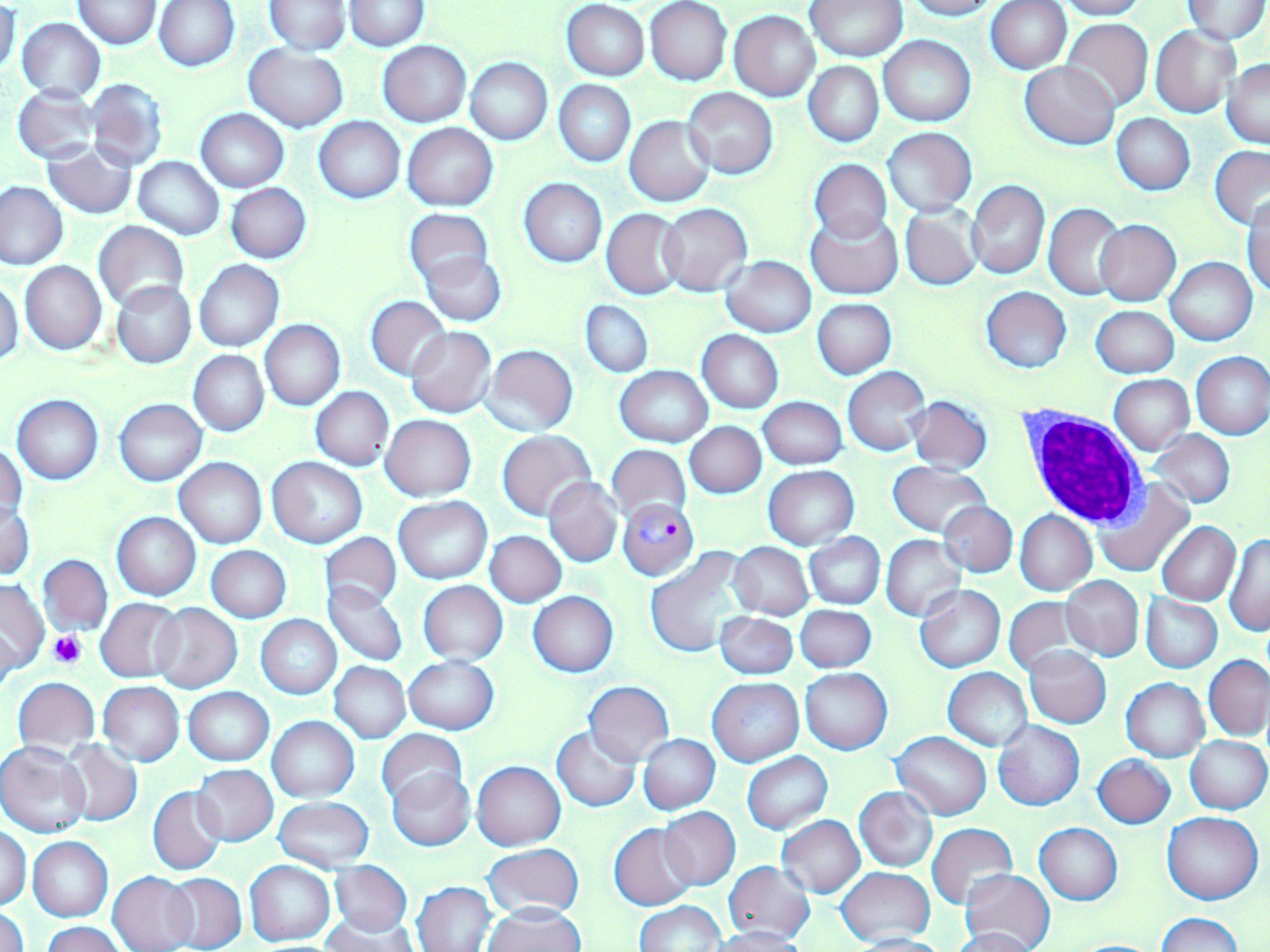
Summary:
  - Coordinate format: approximate bounding boxes as (x1,y1)-(x2,y2) corner pairs in pixels
  - Uninfected red blood cell locations: (73,0)-(162,49), (263,0)-(352,54), (806,0)-(908,63), (901,0)-(1000,20), (1054,0)-(1149,19), (154,1)-(240,72), (344,1)-(429,50), (986,1)-(1070,73), (1181,1)-(1270,43), (563,2)-(649,80), (645,2)-(732,85), (0,4)-(21,81), (729,11)-(820,101), (17,17)-(105,103), (1061,19)-(1154,111), (1151,26)-(1239,118), (878,36)-(975,127), (378,41)-(471,127), (244,45)-(348,131), (466,58)-(552,144), (1224,59)-(1269,147), (805,61)-(883,146), (1021,61)-(1119,150), (85,78)-(169,172), (554,81)-(635,166), (12,86)-(100,163), (681,87)-(778,179), (197,108)-(288,192), (1112,114)-(1194,195), (625,116)-(715,206), (315,117)-(404,203), (403,123)-(497,211), (881,127)-(977,216), (41,141)-(138,218), (1209,147)-(1270,228), (133,156)-(224,239), (809,159)-(893,243), (518,179)-(607,268), (965,179)-(1051,280), (0,181)-(68,270), (226,183)-(312,262), (1245,199)-(1270,299), (659,203)-(752,294), (1044,203)-(1127,299), (901,204)-(982,290), (601,208)-(685,298), (404,209)-(493,292), (806,211)-(901,299), (1095,219)-(1181,306), (93,221)-(189,311), (420,249)-(505,325), (1165,257)-(1257,345), (721,258)-(816,338), (193,259)-(285,352), (20,261)-(107,354), (0,278)-(23,368), (112,281)-(196,369), (981,288)-(1073,372), (366,296)-(450,380), (812,299)-(896,378), (581,301)-(653,377), (1091,305)-(1179,378), (259,319)-(346,410), (404,326)-(496,418), (698,331)-(783,413), (482,345)-(578,437), (188,350)-(269,436), (1192,351)-(1270,440), (615,366)-(712,447), (843,367)-(930,455), (1110,374)-(1194,455), (299,386)-(384,543), (311,387)-(394,471), (12,395)-(104,484), (909,395)-(994,476), (759,397)-(846,469), (115,398)-(207,485), (381,414)-(476,501), (685,421)-(766,498), (1148,429)-(1235,509), (497,431)-(595,520), (1,443)-(26,525), (607,445)-(691,523), (267,457)-(367,548), (174,458)-(266,548), (888,462)-(992,537), (763,466)-(859,548), (544,477)-(622,568), (1092,477)-(1195,578), (395,498)-(492,583), (938,502)-(1016,577), (1,503)-(34,580), (1015,510)-(1096,595), (112,512)-(200,600), (1157,521)-(1240,605), (486,531)-(566,606), (1223,531)-(1270,636), (321,532)-(402,613), (805,533)-(885,608), (881,533)-(966,621), (730,542)-(813,620), (207,546)-(291,622), (646,548)-(755,658), (38,554)-(113,637), (1060,576)-(1145,662), (1,579)-(49,673), (324,581)-(409,667), (418,581)-(507,665), (915,586)-(1005,672), (529,591)-(618,676), (1141,596)-(1222,672), (1003,597)-(1085,676), (96,598)-(185,682), (152,604)-(242,693), (795,606)-(876,672), (715,612)-(798,679), (255,615)-(341,699), (1,624)-(19,702), (1025,646)-(1111,727), (1205,655)-(1270,739), (403,656)-(498,733), (329,662)-(410,743), (800,667)-(892,754), (944,667)-(1032,751), (12,676)-(99,756), (707,677)-(804,766), (1120,678)-(1209,762), (583,681)-(675,766), (97,682)-(184,767), (183,687)-(273,765), (267,716)-(360,801), (993,720)-(1085,812), (552,726)-(641,811), (377,729)-(468,809), (892,732)-(991,819), (638,734)-(720,814), (1185,735)-(1268,814), (62,740)-(142,826), (1,743)-(90,838), (742,752)-(833,833), (1093,754)-(1176,828), (472,761)-(566,850), (191,765)-(277,846), (386,769)-(475,851), (149,786)-(226,876), (854,786)-(938,872), (274,797)-(373,872), (260,800)-(364,930), (660,808)-(741,889), (1163,812)-(1262,905), (777,815)-(865,898), (926,822)-(1018,909), (609,823)-(698,910), (1035,823)-(1122,905), (1,825)-(32,909), (27,837)-(113,921), (483,843)-(585,919), (245,859)-(336,945), (328,861)-(413,936), (722,861)-(815,943), (415,863)-(579,942), (837,867)-(934,944), (961,868)-(1056,952), (108,871)-(198,952), (164,872)-(246,952), (413,881)-(496,951), (634,901)-(724,952), (482,903)-(585,952), (0,905)-(30,952), (1155,913)-(1245,952), (323,915)-(416,952), (43,921)-(125,952), (708,927)-(808,952), (948,928)-(1039,952), (844,933)-(949,952)
  - White blood cell locations: (1017,405)-(1149,530)
  - Platelet locations: (49,629)-(85,668)
  - Plasmodium falciparum-infected red blood cell locations: (616,499)-(698,578)
  - Slide-level diagnosis: Plasmodium falciparum
  - Stain: May-Grünwald-Giemsa
  - Modality: optical microscopy
  - Field of view: one of a larger specimen
  - Magnification: 1000x
  - Preparation: thin blood film
  - Image size: 1270×952 pixels